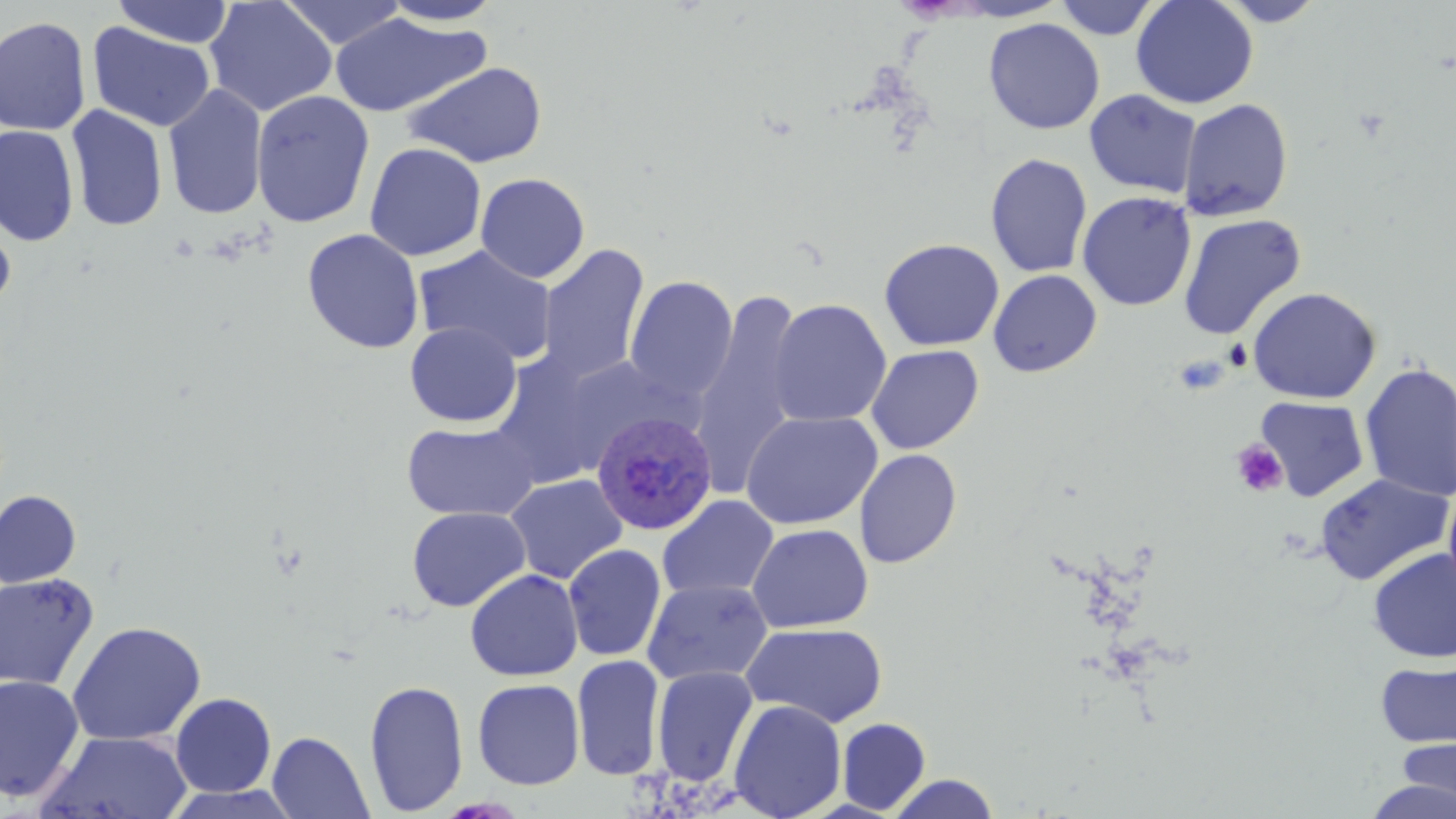
slide-level diagnosis = Plasmodium ovale
image size = 1456×819 pixels
field of view = single
Plasmodium ovale-infected red blood cell locations = approximate bounding boxes as (x1,y1)-(x2,y2) corner pairs in pixels: (591,411)-(717,536)
platelet locations = approximate bounding boxes as (x1,y1)-(x2,y2) corner pairs in pixels: (1224,340)-(1253,370), (1174,354)-(1229,394), (1231,439)-(1288,497)
uninfected red blood cell locations = approximate bounding boxes as (x1,y1)-(x2,y2) corner pairs in pixels: (111,0)-(234,48), (204,0)-(337,117), (279,0)-(407,49), (380,0)-(503,26), (1053,0)-(1162,40), (1131,0)-(1259,109), (1213,0)-(1329,26), (330,13)-(487,118), (0,15)-(92,136), (984,17)-(1104,135), (87,22)-(215,132), (403,61)-(547,168), (163,84)-(268,220), (1084,89)-(1202,198), (251,90)-(374,228), (1178,98)-(1294,222), (66,105)-(169,232), (0,124)-(79,246), (364,142)-(486,262), (985,152)-(1093,278), (476,172)-(590,283), (1077,190)-(1197,312), (0,214)-(16,317), (1178,214)-(1306,340), (302,229)-(424,354), (879,238)-(1005,351), (537,244)-(650,384), (414,245)-(558,366), (988,270)-(1101,377), (624,275)-(738,402), (1247,286)-(1381,404), (691,287)-(806,495), (767,299)-(892,428), (405,321)-(522,427), (866,345)-(984,454), (488,352)-(620,489), (1359,361)-(1456,503), (1255,396)-(1370,502), (741,411)-(882,530), (401,421)-(540,521), (854,449)-(962,569), (1314,473)-(1455,586), (504,474)-(627,584), (1443,483)-(1456,602), (0,490)-(82,588), (657,495)-(778,600), (406,506)-(531,612), (747,523)-(873,633), (563,544)-(666,661), (1368,548)-(1456,663), (465,568)-(583,681), (0,572)-(100,691), (642,578)-(773,686), (67,620)-(206,745), (741,623)-(888,728), (570,654)-(665,780), (1375,658)-(1456,749), (652,665)-(758,787), (0,675)-(85,803), (472,678)-(585,790), (364,679)-(469,816), (171,693)-(276,797), (729,700)-(847,819), (837,717)-(931,814), (35,730)-(194,818), (267,731)-(374,818), (1395,733)-(1456,812), (887,773)-(1000,818), (1362,777)-(1456,819), (163,785)-(303,819)
stain = May-Grünwald-Giemsa
magnification = 1000x
modality = light microscopy
preparation = thin blood film